State which cell type is depicted.
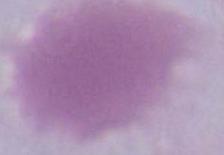
This is an erythrocyte.

modality = photomicrograph
magnification = 1000x